Describe the morphology of the red blood cells.
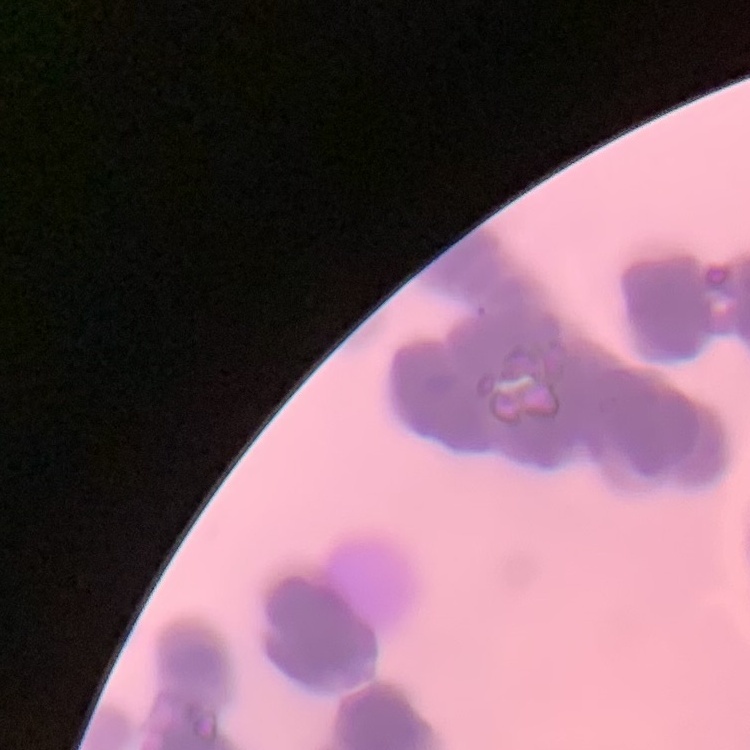

They show rouleaux formation.

{
  "stain": "Field's or Giemsa",
  "preparation": "thin peripheral smear",
  "image_type": "one tile cut from a larger photomicrograph"
}